Identify the preparation type.
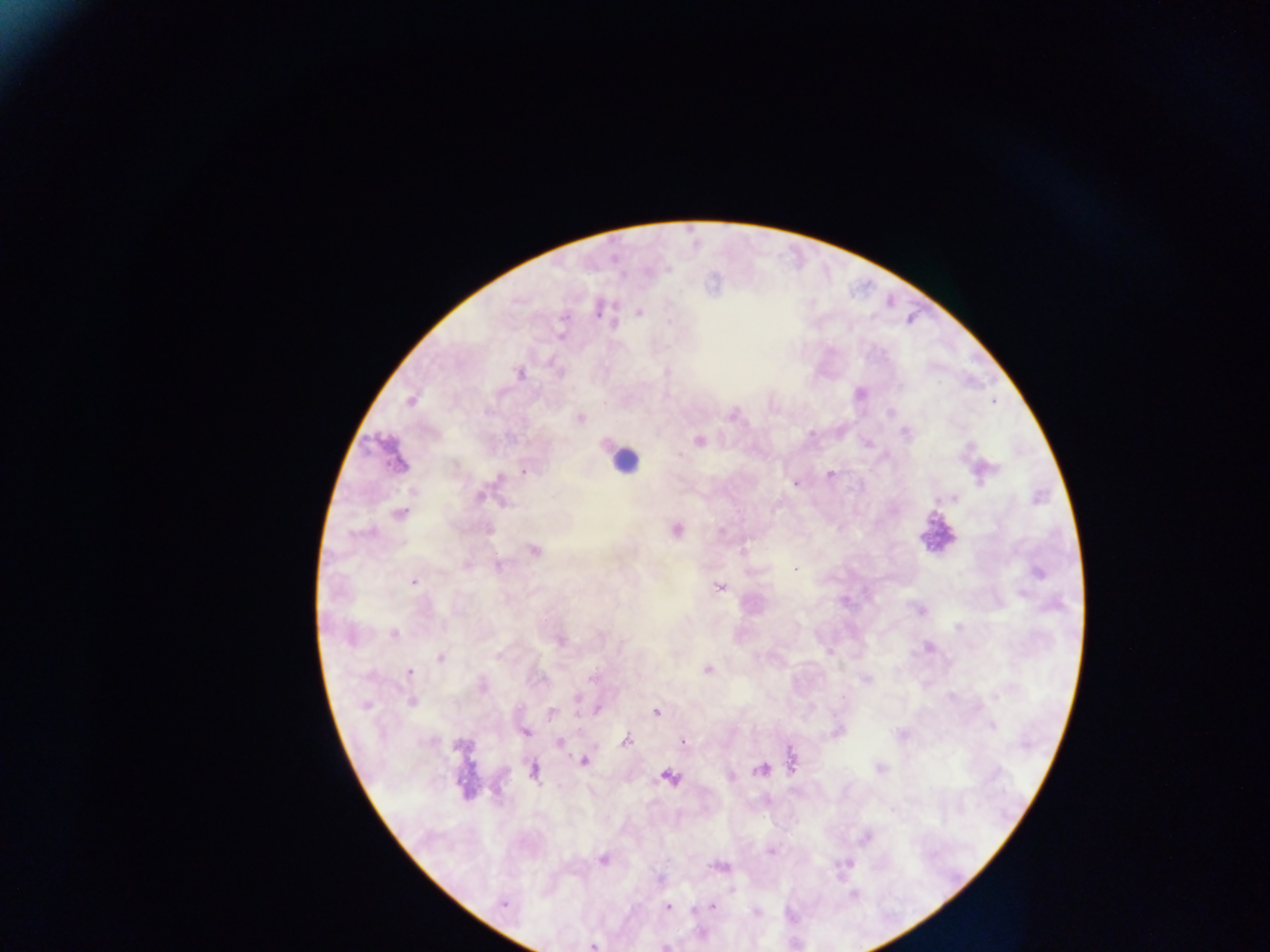

Thick blood film.

Approximate centers as (x, y) in pixels.
Summary:
  - Plasmodium parasite locations: (598, 310), (639, 313), (563, 318), (561, 335), (667, 372), (520, 373), (860, 394), (410, 401), (994, 403), (890, 412), (580, 418), (906, 433), (699, 440), (524, 472), (830, 474), (499, 477), (795, 484), (479, 497), (953, 498), (504, 504), (398, 514), (677, 530), (722, 531), (534, 550), (742, 552), (466, 565), (498, 566), (795, 570), (1037, 572), (414, 582), (719, 587), (920, 610), (958, 627), (394, 634), (559, 641), (929, 647), (496, 655), (441, 657), (707, 669), (410, 672), (591, 679), (866, 680), (482, 686), (577, 697), (996, 697), (412, 701), (364, 706), (597, 710), (551, 712), (656, 713), (992, 726), (838, 731), (526, 732), (900, 734), (626, 741), (559, 742), (683, 742), (459, 746), (791, 759), (585, 761), (880, 768), (761, 769), (533, 771), (669, 777), (731, 777), (866, 838), (771, 852), (604, 859), (719, 866), (732, 890), (503, 903), (668, 906), (711, 906), (755, 911), (592, 946)
  - Leukocyte locations: (625, 462), (936, 533)
  - Image size: 1270×952 pixels
  - Field of view: single
  - Country: Ghana
  - Capture: mobile-phone photograph through a microscope